Name the cell type shown.
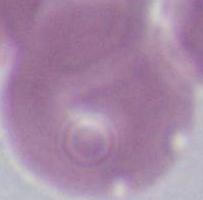
An erythrocyte.

1000x magnification. Micrograph.